Assess this cell for malaria.
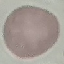

It is uninfected.

Acquired by smartphone through the microscope eyepiece. Thin blood film. Automatically extracted cell patch, resized to 64 × 64 pixels. Giemsa stain.